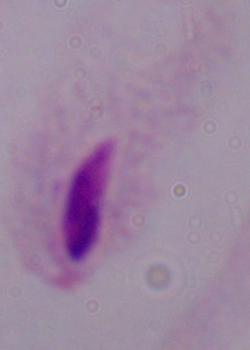

Summary:
  - Identification: trichomonad
  - Modality: micrograph
  - Magnification: 1000x